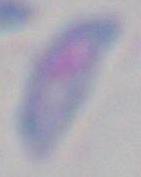
Summary:
  - Modality: photomicrograph
  - Identification: Toxoplasma gondii
  - Magnification: 1000x